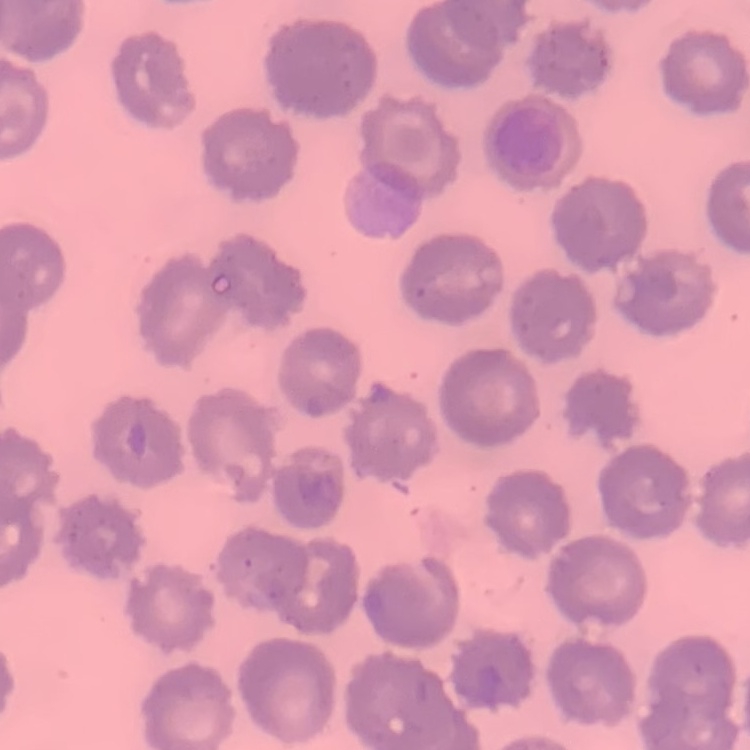 The erythrocytes exhibit no rouleaux formation. Field's or Giemsa stain. Square crop of a larger photomicrograph. Thin blood smear.